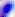

magnification = 400x
identification = Toxoplasma gondii
modality = micrograph